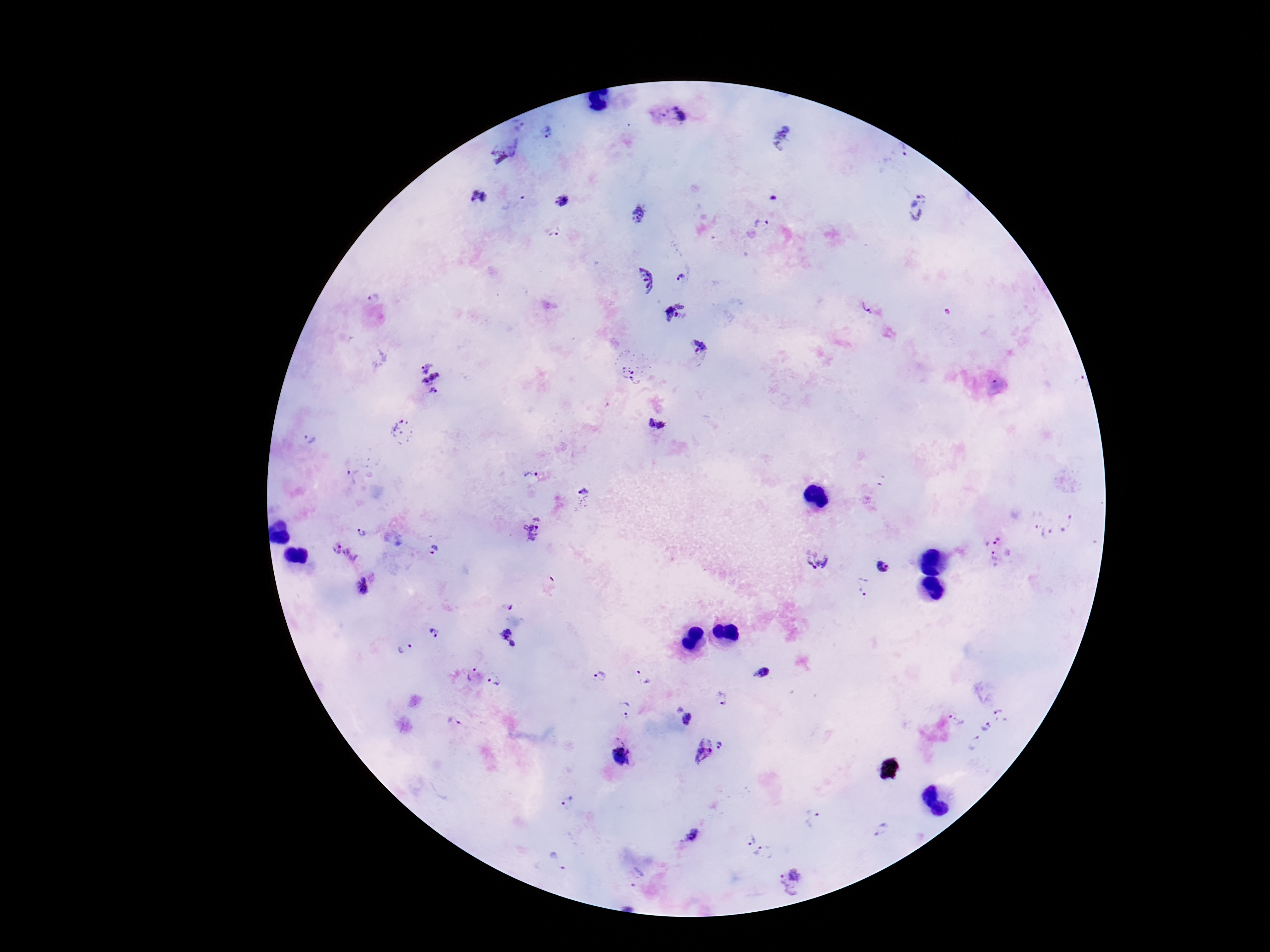
Approximate centers as [x, y] in pixels. Plasmodium parasite locations: [672, 116], [517, 124], [546, 132], [782, 137], [898, 151], [509, 153], [481, 197], [562, 201], [920, 208], [640, 214], [761, 223], [553, 233], [681, 276], [642, 280], [866, 304], [674, 311], [700, 349], [630, 375], [430, 378], [656, 424], [403, 433], [309, 440], [352, 475], [531, 478], [584, 492], [1068, 523], [532, 530], [1042, 530], [363, 533], [995, 539], [433, 549], [344, 553], [994, 558], [816, 559], [884, 568], [364, 586], [866, 586], [510, 607], [505, 631], [434, 632], [513, 644], [404, 648], [762, 672], [471, 675], [642, 676], [600, 677], [495, 679], [724, 698], [626, 710], [684, 713], [1002, 715], [956, 720], [454, 722], [985, 727], [720, 744], [974, 744], [704, 748], [622, 757], [567, 800], [814, 819], [881, 829], [749, 839], [764, 854], [557, 863], [637, 877], [793, 882]. Image is 1270×952 pixels. Giemsa-stained preparation. Patient malaria status: infected. Thick peripheral-blood smear. Single field of view. 100x magnification. Photographed through the microscope eyepiece with a smartphone camera.